Identify the blood parasite species.
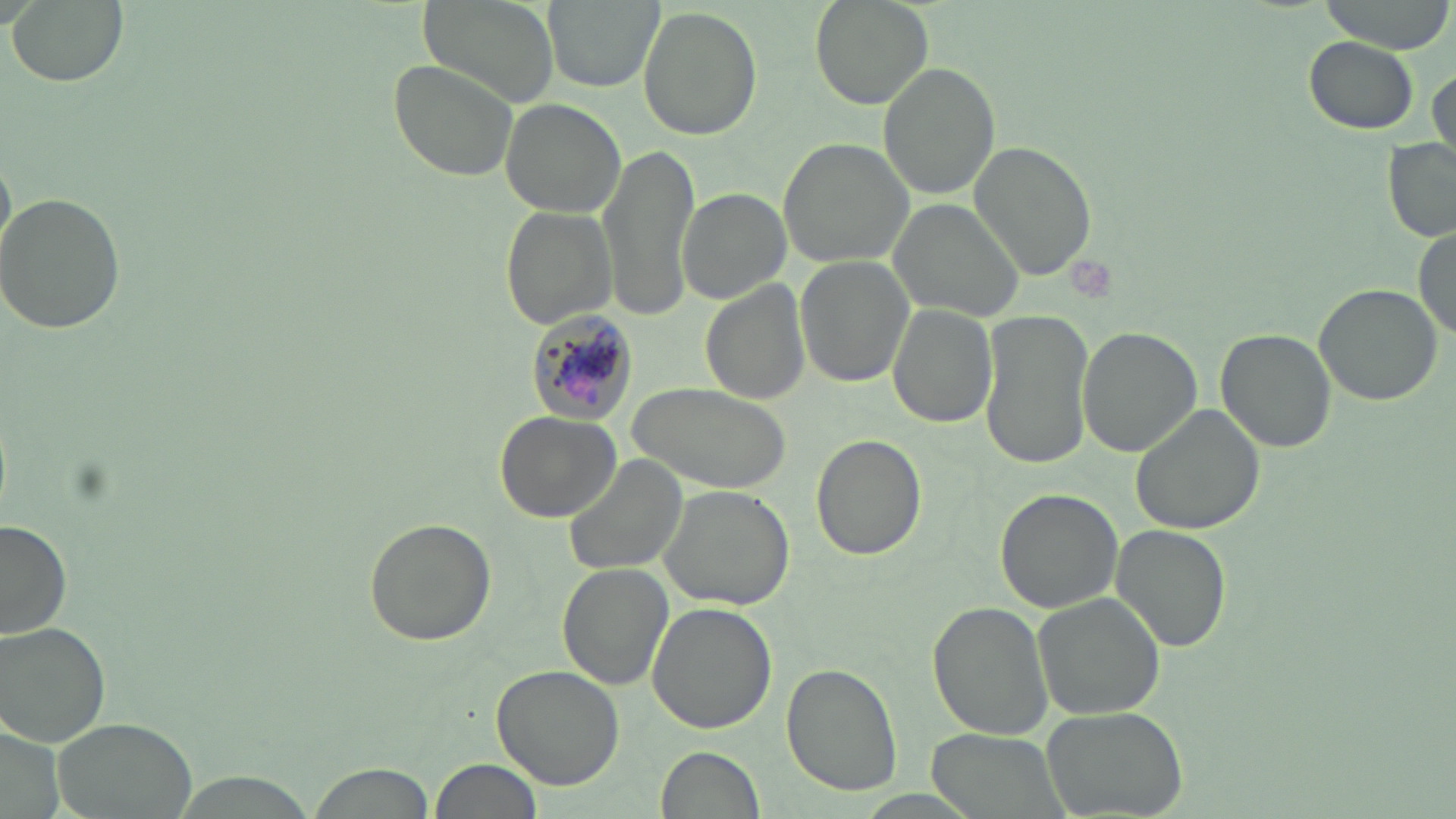
Plasmodium malariae.

Approximate bounding boxes as (x1, y1, x2, y2) in pixels. Plasmodium malariae-infected red blood cell locations: (519, 305, 638, 424). Uninfected red blood cell locations: (6, 0, 128, 87), (416, 0, 558, 110), (543, 0, 662, 92), (810, 0, 933, 109), (637, 7, 763, 141), (1302, 36, 1419, 135), (386, 58, 519, 182), (878, 62, 999, 199), (1428, 65, 1454, 166), (500, 100, 625, 219), (777, 137, 915, 267), (968, 139, 1098, 281), (1385, 139, 1456, 246), (596, 140, 701, 320), (678, 188, 791, 306), (1, 192, 127, 334), (887, 198, 1028, 323), (501, 206, 617, 330), (1415, 222, 1455, 343), (794, 255, 915, 389), (701, 279, 809, 404), (1313, 282, 1443, 405), (886, 302, 998, 428), (979, 310, 1095, 472), (663, 323, 811, 471), (1076, 326, 1204, 458), (1216, 328, 1338, 453), (631, 383, 789, 490), (1130, 403, 1267, 537), (493, 410, 624, 523), (811, 432, 926, 561), (563, 453, 689, 577), (657, 485, 795, 611), (994, 488, 1122, 614), (362, 516, 497, 648), (0, 520, 74, 641), (1109, 524, 1233, 653), (556, 565, 672, 693), (1033, 593, 1166, 721), (647, 602, 777, 735), (928, 603, 1054, 741), (1, 618, 113, 745), (781, 663, 902, 797), (492, 664, 626, 790), (1041, 705, 1189, 819), (50, 717, 199, 819), (922, 729, 1072, 817), (657, 746, 767, 819), (432, 758, 541, 819), (307, 762, 436, 819), (166, 771, 317, 819). Platelet locations: (1066, 254, 1120, 307). Light microscopy. Single field of view. Image is 1456×819 pixels. Thin blood smear. 1000x magnification. May-Grünwald-Giemsa-stained preparation.